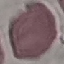

Summary:
  - Result: no malaria parasites seen
  - Image type: cell patch, automatically extracted from a larger field of view and resized to 64 × 64 pixels
  - Stain: Giemsa
  - Preparation: thin smear
  - Capture: smartphone through the microscope eyepiece